State the preparation type.
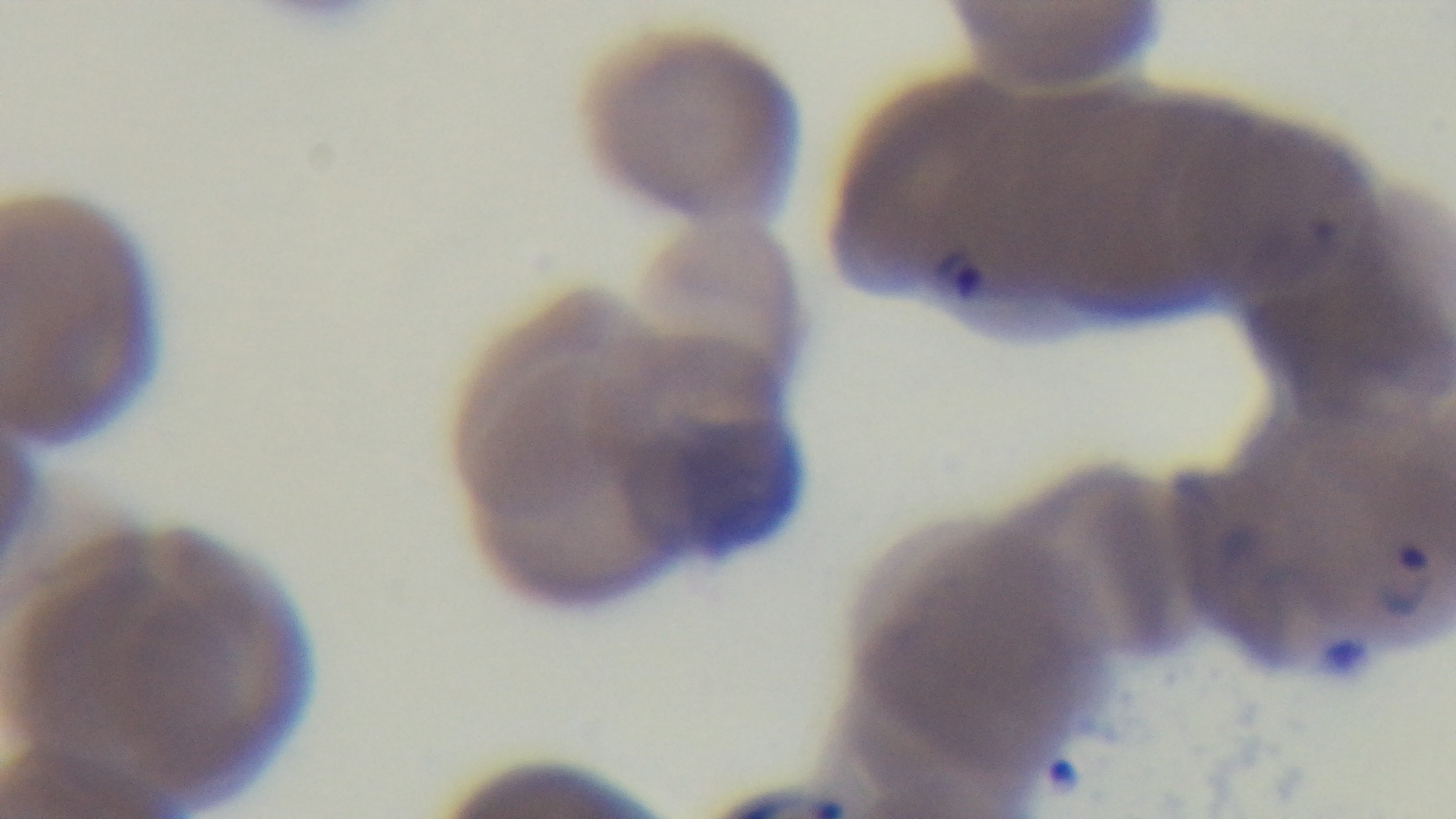

A thin smear.

Summary:
  - Objective: 100x oil immersion
  - Modality: light microscopy
  - Field of view: one from the slide
  - Stain: Giemsa
  - Malaria status: infected
  - Capture: mounted 4K digital camera